Report the malaria status of this cell.
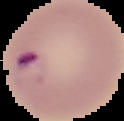

It is parasitized.

Segmented cell region on a black background. Image is 124×121 pixels. From a thin blood film.